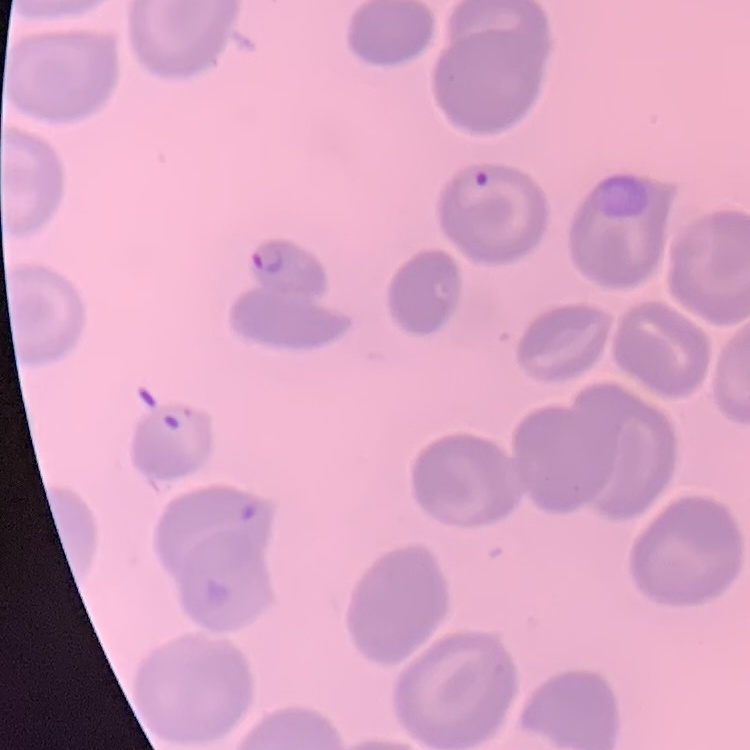
The erythrocytes exhibit no rouleaux formation. Thin peripheral smear. Field's or Giemsa stain. Square crop of a larger photomicrograph.